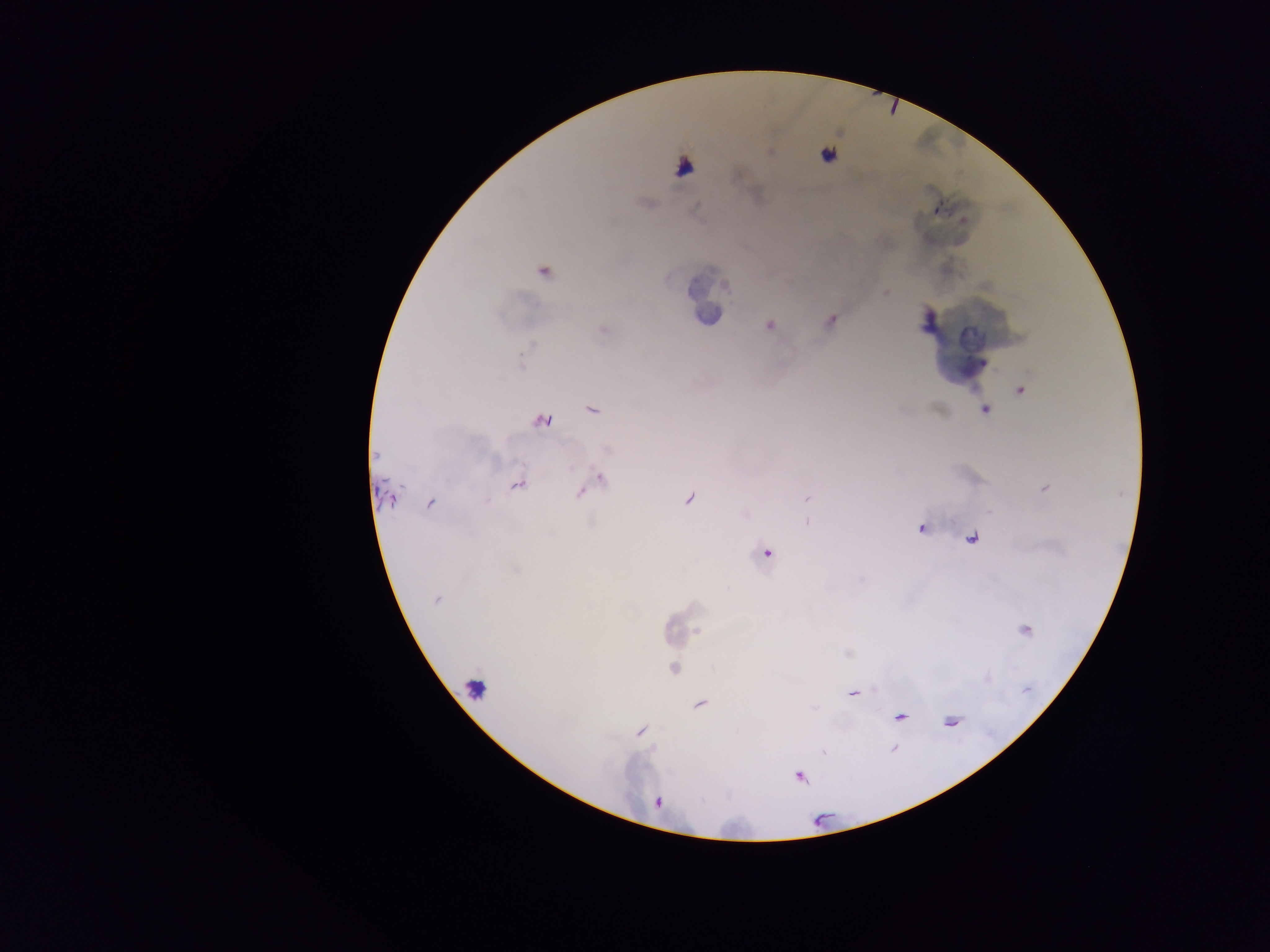 Approximate centers as {x, y} in pixels. Leukocyte locations: {683, 167}, {705, 312}, {474, 687}. Malaria parasite locations: {827, 155}, {936, 209}, {543, 270}, {884, 292}, {830, 320}, {769, 324}, {602, 329}, {1020, 390}, {592, 409}, {984, 409}, {541, 420}, {601, 477}, {517, 483}, {1043, 488}, {582, 491}, {387, 495}, {689, 498}, {807, 499}, {431, 503}, {807, 519}, {922, 528}, {971, 538}, {766, 552}, {436, 599}, {1024, 630}, {673, 668}, {853, 692}, {699, 704}, {900, 717}, {950, 721}, {641, 731}, {799, 775}, {657, 802}. One field of view. Thick blood film. Collected in Ghana. Photographed through a microscope with a mobile-phone camera. Image is 1270×952 pixels.